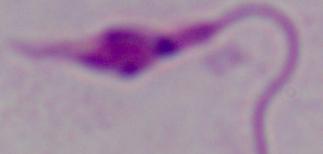 Captured at 1000x magnification. Micrograph. A Leishmania parasite is shown.